Point out each leukocyte.
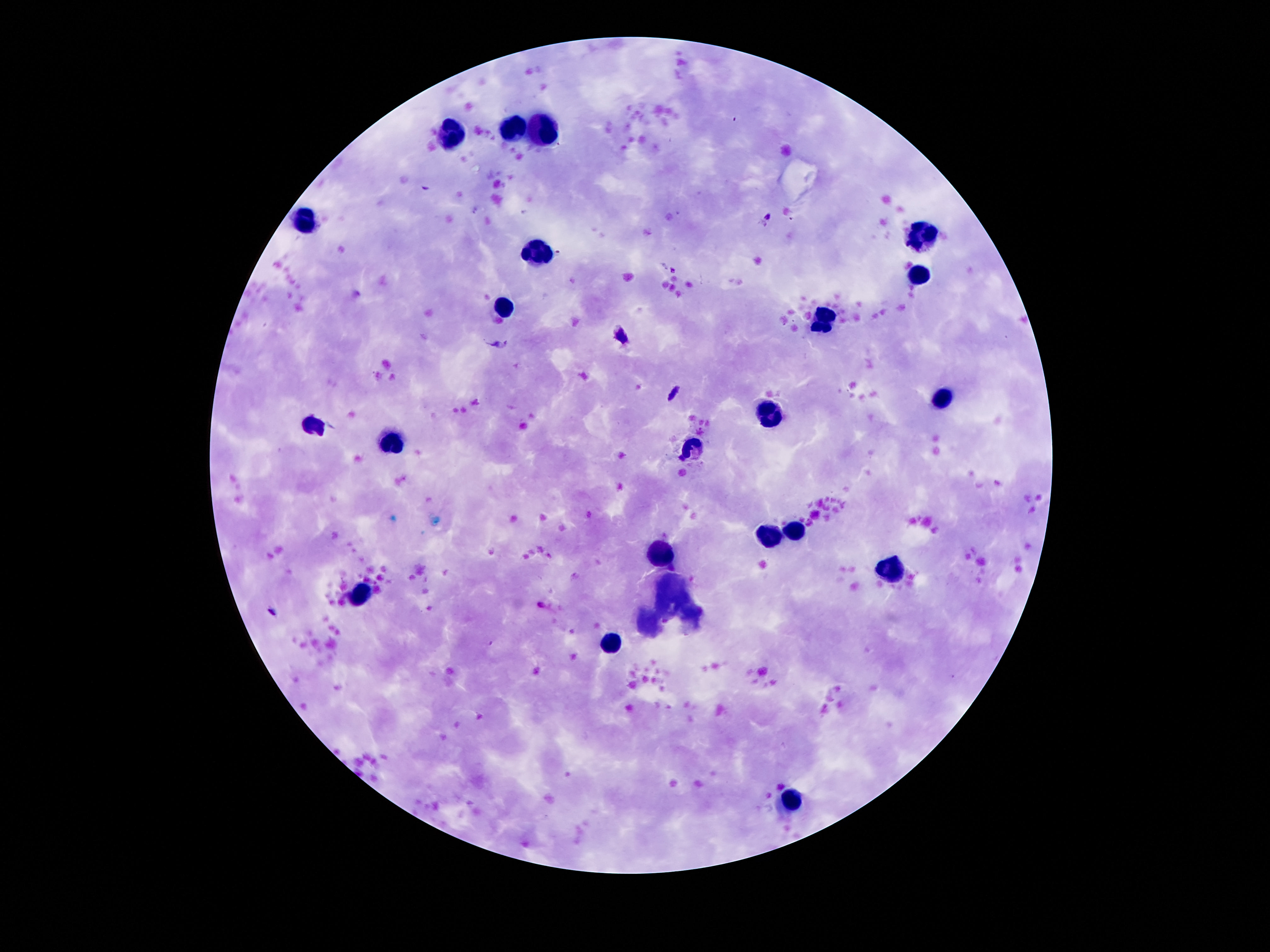
Approximate centers as [x, y] in pixels.
Leukocytes: [515, 127], [543, 127], [447, 133], [303, 219], [923, 235], [537, 255], [915, 275], [503, 305], [823, 321], [943, 397], [769, 413], [313, 427], [389, 441], [691, 449], [795, 533], [767, 535], [663, 551], [893, 569], [363, 591], [615, 639], [793, 799].

Thick blood smear. Smartphone photograph taken through the microscope eyepiece. Image is 1270×952 pixels. One field from this slide. 100x magnification. Patient malaria status: not infected. Giemsa-stained preparation.